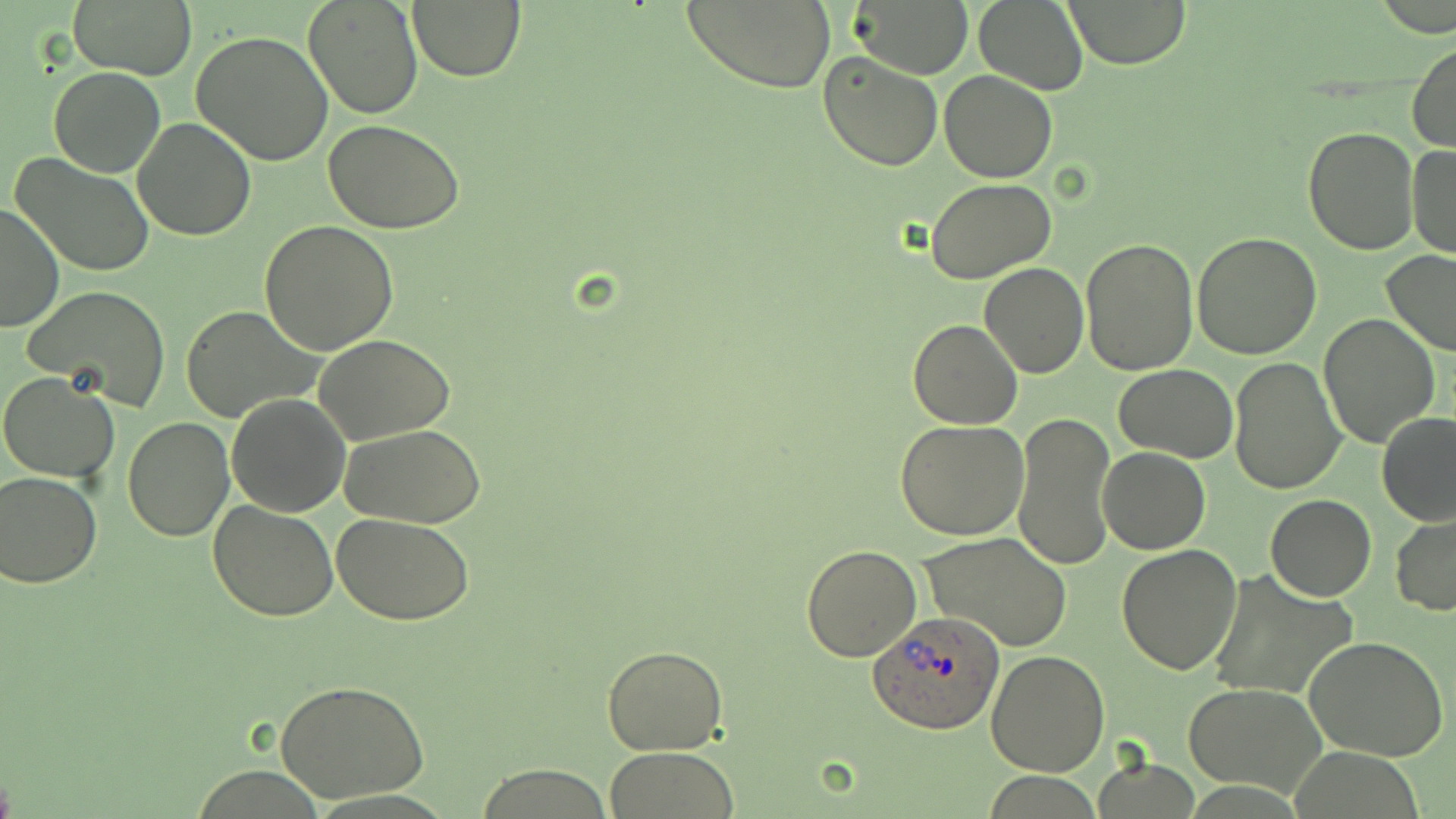
Approximate bounding boxes as [x1, y1, x2, y2] in pixels. Plasmodium ovale-infected red blood cell locations: [869, 611, 1006, 733]. Uninfected red blood cell locations: [303, 0, 424, 120], [407, 0, 525, 82], [679, 0, 835, 92], [972, 0, 1089, 94], [1062, 0, 1191, 69], [69, 1, 196, 79], [854, 2, 971, 74], [192, 30, 334, 165], [1407, 41, 1456, 153], [818, 50, 944, 172], [47, 66, 166, 177], [939, 70, 1057, 182], [132, 117, 256, 241], [322, 119, 466, 236], [1303, 127, 1417, 255], [1406, 144, 1455, 259], [11, 152, 155, 277], [927, 179, 1057, 283], [1, 202, 62, 334], [259, 219, 400, 356], [1192, 231, 1323, 359], [1080, 238, 1198, 375], [1381, 251, 1456, 358], [978, 263, 1089, 378], [22, 284, 173, 411], [181, 306, 326, 424], [1318, 312, 1439, 448], [908, 319, 1023, 429], [315, 334, 456, 444], [1228, 355, 1346, 494], [1115, 366, 1239, 462], [0, 371, 120, 482], [225, 395, 349, 518], [1012, 411, 1116, 570], [1375, 411, 1456, 526], [123, 417, 234, 540], [895, 419, 1028, 539], [341, 425, 486, 528], [1097, 447, 1210, 555], [0, 470, 102, 586], [1266, 493, 1376, 601], [209, 501, 338, 621], [333, 514, 477, 625], [1391, 514, 1456, 615], [920, 532, 1073, 651], [800, 543, 923, 662], [1117, 543, 1242, 675], [1209, 566, 1357, 701], [1303, 633, 1450, 761], [602, 643, 729, 754], [985, 648, 1111, 776], [278, 680, 429, 806], [1183, 683, 1326, 797], [607, 746, 738, 819], [1094, 758, 1199, 817], [474, 765, 615, 819], [984, 773, 1104, 817]. Slide-level diagnosis: Plasmodium ovale. Single field of view. Optical microscopy. Thin blood smear. 1000x magnification. May-Grünwald-Giemsa stain. Image is 1456×819 pixels.